Classify this cell by malaria status.
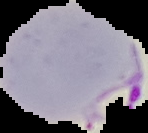
Parasitized.

Summary:
  - Image type: segmented cell region on a black background
  - Preparation: thin blood film
  - Image size: 148×133 pixels